Comment on the morphology of the red blood cells.
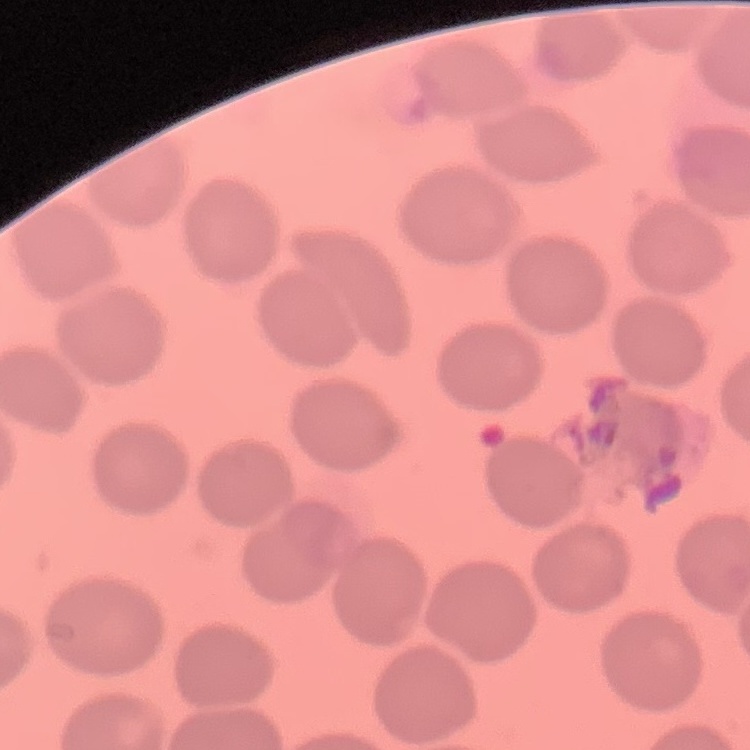
They show no rouleaux formation.

image type = one tile cut from a larger photomicrograph
stain = Field's or Giemsa
preparation = thin blood film